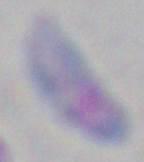
Summary:
  - Identification: Toxoplasma gondii
  - Modality: photomicrograph
  - Magnification: 1000x